Report the malaria status of this cell.
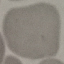
It is uninfected.

Summary:
  - Stain: Giemsa
  - Capture: smartphone camera at the microscope eyepiece
  - Preparation: thin blood smear
  - Image type: cell patch, automatically extracted from a larger field of view and resized to 64 × 64 pixels